Classify the preparation.
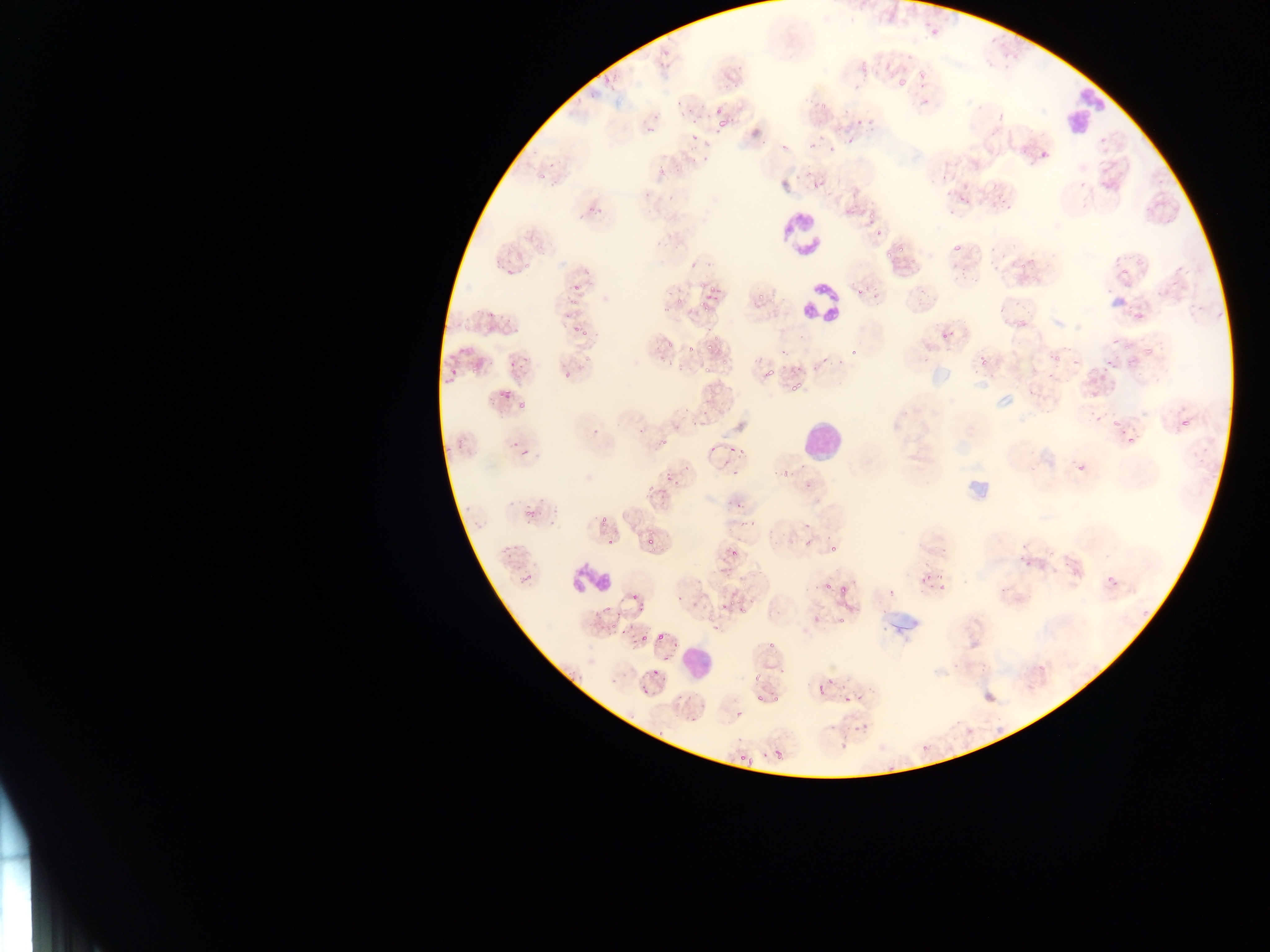
This is a thin smear.

Approximate bounding boxes as [left, top, right, bottom] in pixels.
Summary:
  - Artifact (stain precipitate or debris) locations: [943, 453, 994, 506], [870, 590, 920, 648]
  - Plasmodium parasite locations (subset; some below the resolvable size): [929, 27, 939, 35], [917, 66, 927, 81], [859, 68, 867, 75], [896, 73, 910, 88], [589, 93, 599, 101], [819, 101, 827, 112], [713, 108, 721, 115], [679, 110, 685, 120], [653, 114, 659, 122], [718, 115, 734, 126], [855, 118, 864, 127], [645, 127, 655, 133], [712, 130, 718, 138], [847, 135, 853, 145], [781, 141, 786, 155], [827, 143, 836, 153], [686, 147, 697, 151], [1038, 151, 1047, 160], [691, 157, 699, 164], [549, 161, 555, 169], [657, 166, 665, 174], [536, 171, 550, 182], [812, 180, 819, 189], [643, 192, 651, 198], [1006, 204, 1014, 212], [868, 213, 873, 221], [870, 227, 888, 240], [952, 242, 962, 255], [537, 243, 547, 250], [898, 244, 903, 255], [885, 251, 893, 258], [1020, 259, 1031, 268], [493, 260, 502, 269], [692, 261, 701, 269], [507, 268, 515, 275], [1120, 270, 1130, 277], [573, 276, 581, 292], [700, 280, 706, 288], [855, 286, 866, 297], [874, 288, 880, 299], [757, 291, 765, 298], [712, 294, 718, 303], [568, 298, 579, 304], [677, 300, 685, 306], [705, 303, 712, 311], [562, 310, 570, 320], [486, 312, 496, 321], [505, 315, 514, 323], [455, 322, 464, 326], [573, 323, 579, 332], [513, 328, 521, 336], [582, 330, 590, 336], [668, 341, 676, 350], [1123, 341, 1134, 351], [687, 344, 694, 354], [707, 344, 716, 351], [1145, 345, 1156, 353], [851, 347, 859, 357], [583, 350, 592, 363], [448, 351, 459, 359], [1055, 351, 1063, 361], [520, 352, 525, 363], [981, 356, 985, 368], [488, 358, 495, 366], [1103, 358, 1112, 366], [450, 365, 458, 374], [471, 365, 479, 373], [765, 365, 778, 378], [703, 368, 711, 373], [443, 374, 454, 384], [791, 379, 803, 392], [499, 389, 512, 398], [518, 400, 525, 411], [683, 405, 690, 413], [1172, 412, 1195, 438], [693, 418, 701, 428], [1112, 419, 1120, 425], [638, 424, 648, 436], [1119, 426, 1144, 452], [590, 427, 601, 434], [512, 440, 518, 449], [660, 440, 670, 444], [519, 449, 533, 457], [739, 449, 745, 457], [686, 462, 689, 472], [1075, 462, 1085, 472], [731, 466, 742, 478], [782, 468, 787, 478], [666, 469, 673, 480], [675, 476, 684, 484], [806, 482, 813, 490], [647, 483, 655, 492], [737, 501, 743, 509], [525, 507, 535, 515], [524, 514, 532, 524], [599, 514, 605, 525], [749, 522, 757, 528], [803, 522, 813, 533], [645, 536, 653, 544], [608, 537, 615, 545], [831, 546, 839, 554], [507, 552, 512, 560], [1101, 569, 1123, 593], [937, 572, 945, 579], [826, 583, 834, 591], [841, 584, 849, 594], [939, 585, 947, 591], [630, 587, 638, 600], [678, 592, 684, 601], [734, 596, 742, 604], [748, 600, 757, 604], [720, 602, 728, 610], [636, 604, 647, 613], [601, 608, 611, 614], [739, 608, 747, 613], [814, 619, 823, 627], [710, 622, 720, 631], [611, 623, 618, 633], [657, 628, 671, 644], [638, 636, 647, 644], [673, 637, 682, 648], [768, 641, 778, 650], [650, 662, 661, 676], [776, 668, 785, 674], [754, 673, 763, 684], [828, 678, 833, 690], [842, 683, 847, 691], [818, 685, 824, 694], [641, 688, 650, 695], [856, 694, 865, 702], [843, 696, 851, 707], [735, 709, 747, 721], [828, 723, 837, 732], [853, 724, 858, 732], [837, 743, 847, 749], [775, 752, 783, 759], [739, 754, 748, 760], [748, 755, 757, 767], [884, 767, 893, 771] | approximate [x, y] pixel centers of objects too small to bound: [666, 55], [661, 65], [607, 79], [678, 102], [689, 110], [696, 123], [693, 139], [763, 143], [810, 145], [705, 158], [676, 167], [672, 200], [961, 200], [1003, 201], [598, 208], [590, 210], [510, 254], [528, 264], [712, 292], [702, 306], [666, 308], [943, 336], [716, 337], [1113, 341], [783, 354], [726, 361], [1075, 362], [513, 365], [679, 367], [1105, 368], [567, 374], [705, 414], [461, 441], [448, 448], [731, 448], [712, 449], [556, 509], [477, 522], [551, 523], [809, 546], [733, 554], [530, 577], [927, 577], [842, 619], [623, 634], [612, 679], [665, 681], [680, 696], [759, 698], [775, 699], [696, 721], [865, 727], [661, 734], [924, 748]
  - Leukocyte locations: [1053, 69, 1104, 150], [764, 198, 824, 255], [795, 279, 844, 331], [797, 416, 848, 466], [572, 565, 614, 597], [679, 640, 716, 679]
  - Country: Ghana
  - Capture: mobile-phone photograph through a microscope
  - Field of view: single
  - Image size: 1270×952 pixels